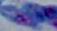
magnification: 1000x
identification: Toxoplasma gondii
modality: micrograph